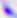

modality = micrograph
identification = Toxoplasma gondii
magnification = 400x